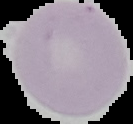

Summary:
  - Result: no Plasmodium parasites seen
  - Image size: 133×124 pixels
  - Image type: segmented cell region on a black background
  - Preparation: thin blood film